Locate every blood parasite and identify its species.
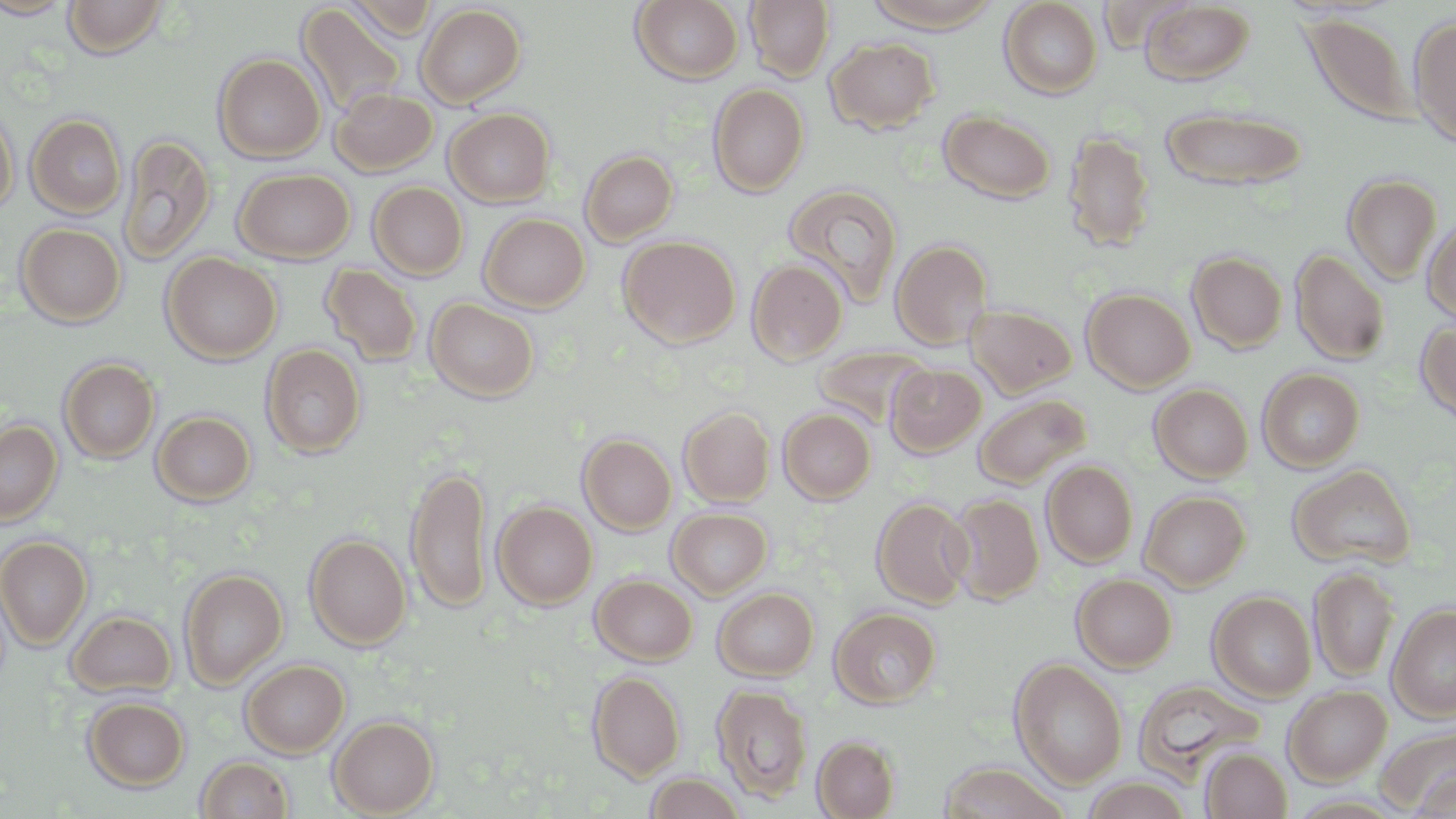

No blood parasites seen.

slide-level diagnosis = negative for blood parasites
preparation = thin blood smear
uninfected red blood cell locations = approximate bounding boxes as named x1/y1/x2/y2 corners in pixels: (x1=0, y1=0, x2=78, y2=19), (x1=343, y1=0, x2=437, y2=40), (x1=631, y1=0, x2=744, y2=84), (x1=745, y1=0, x2=835, y2=82), (x1=863, y1=0, x2=1003, y2=32), (x1=999, y1=0, x2=1103, y2=99), (x1=63, y1=1, x2=168, y2=58), (x1=1139, y1=1, x2=1255, y2=86), (x1=296, y1=4, x2=406, y2=118), (x1=416, y1=4, x2=526, y2=107), (x1=1300, y1=13, x2=1418, y2=126), (x1=1408, y1=15, x2=1456, y2=147), (x1=826, y1=37, x2=939, y2=134), (x1=214, y1=53, x2=325, y2=162), (x1=708, y1=83, x2=809, y2=196), (x1=330, y1=88, x2=438, y2=176), (x1=1160, y1=106, x2=1308, y2=191), (x1=0, y1=107, x2=17, y2=215), (x1=444, y1=107, x2=555, y2=206), (x1=939, y1=110, x2=1055, y2=203), (x1=27, y1=113, x2=126, y2=219), (x1=1062, y1=129, x2=1156, y2=252), (x1=118, y1=134, x2=216, y2=265), (x1=580, y1=149, x2=678, y2=245), (x1=233, y1=168, x2=355, y2=263), (x1=1343, y1=174, x2=1442, y2=285), (x1=368, y1=182, x2=468, y2=280), (x1=782, y1=183, x2=903, y2=306), (x1=479, y1=213, x2=589, y2=312), (x1=1422, y1=214, x2=1456, y2=325), (x1=15, y1=222, x2=126, y2=327), (x1=619, y1=235, x2=741, y2=347), (x1=890, y1=239, x2=994, y2=350), (x1=1291, y1=248, x2=1390, y2=365), (x1=1187, y1=251, x2=1288, y2=353), (x1=162, y1=252, x2=282, y2=364), (x1=747, y1=259, x2=848, y2=365), (x1=321, y1=263, x2=423, y2=366), (x1=1082, y1=288, x2=1195, y2=393), (x1=426, y1=298, x2=539, y2=402), (x1=965, y1=303, x2=1077, y2=398), (x1=1415, y1=319, x2=1456, y2=425), (x1=261, y1=344, x2=367, y2=458), (x1=814, y1=345, x2=931, y2=429), (x1=59, y1=358, x2=159, y2=463), (x1=886, y1=363, x2=986, y2=457), (x1=1258, y1=367, x2=1364, y2=472), (x1=1150, y1=384, x2=1253, y2=483), (x1=973, y1=393, x2=1091, y2=489), (x1=679, y1=406, x2=775, y2=506), (x1=779, y1=408, x2=876, y2=503), (x1=152, y1=410, x2=255, y2=505), (x1=0, y1=420, x2=62, y2=525), (x1=578, y1=433, x2=677, y2=535), (x1=1041, y1=460, x2=1138, y2=567), (x1=405, y1=463, x2=491, y2=614), (x1=1287, y1=463, x2=1416, y2=570), (x1=1139, y1=490, x2=1250, y2=590), (x1=946, y1=493, x2=1044, y2=604), (x1=872, y1=497, x2=974, y2=608), (x1=492, y1=500, x2=597, y2=610), (x1=667, y1=508, x2=771, y2=599), (x1=305, y1=534, x2=411, y2=649), (x1=0, y1=535, x2=92, y2=649), (x1=1309, y1=566, x2=1399, y2=682), (x1=179, y1=568, x2=288, y2=687), (x1=1072, y1=573, x2=1177, y2=672), (x1=591, y1=574, x2=697, y2=665), (x1=714, y1=587, x2=819, y2=680), (x1=1208, y1=591, x2=1316, y2=702), (x1=1387, y1=603, x2=1456, y2=721), (x1=830, y1=606, x2=941, y2=708), (x1=66, y1=609, x2=177, y2=698), (x1=1009, y1=658, x2=1128, y2=788), (x1=241, y1=659, x2=349, y2=757), (x1=588, y1=671, x2=685, y2=782), (x1=1133, y1=678, x2=1266, y2=781), (x1=712, y1=684, x2=813, y2=801), (x1=1283, y1=685, x2=1392, y2=785), (x1=83, y1=697, x2=190, y2=791), (x1=329, y1=716, x2=439, y2=817), (x1=1377, y1=725, x2=1456, y2=813), (x1=813, y1=736, x2=899, y2=818), (x1=1200, y1=746, x2=1292, y2=818), (x1=196, y1=756, x2=294, y2=818), (x1=936, y1=761, x2=1070, y2=819), (x1=645, y1=772, x2=746, y2=818), (x1=1079, y1=775, x2=1194, y2=818)
image size = 1456×819 pixels
modality = light microscopy
field of view = one of a larger specimen
magnification = 1000x
stain = May-Grünwald-Giemsa